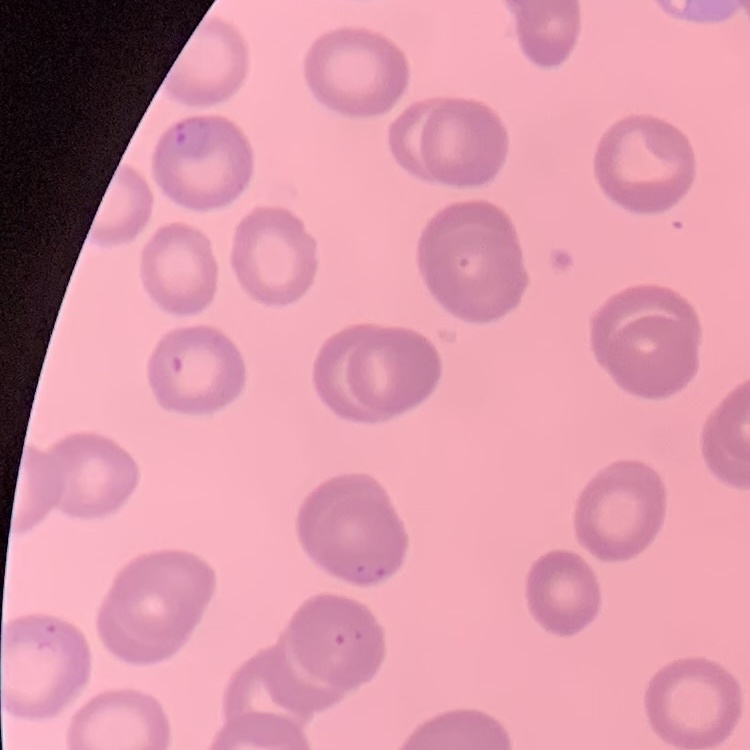

Summary:
  - Red blood cell morphology: no rouleaux formation
  - Image type: square crop of a larger photomicrograph
  - Stain: Field's or Giemsa
  - Preparation: thin blood smear